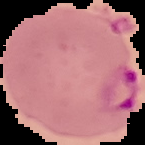
image_size: 145×145 pixels
malaria_status: parasitized
image_type: segmented cell region on a black background
preparation: thin blood smear